Evaluate for parasitized red blood cells.
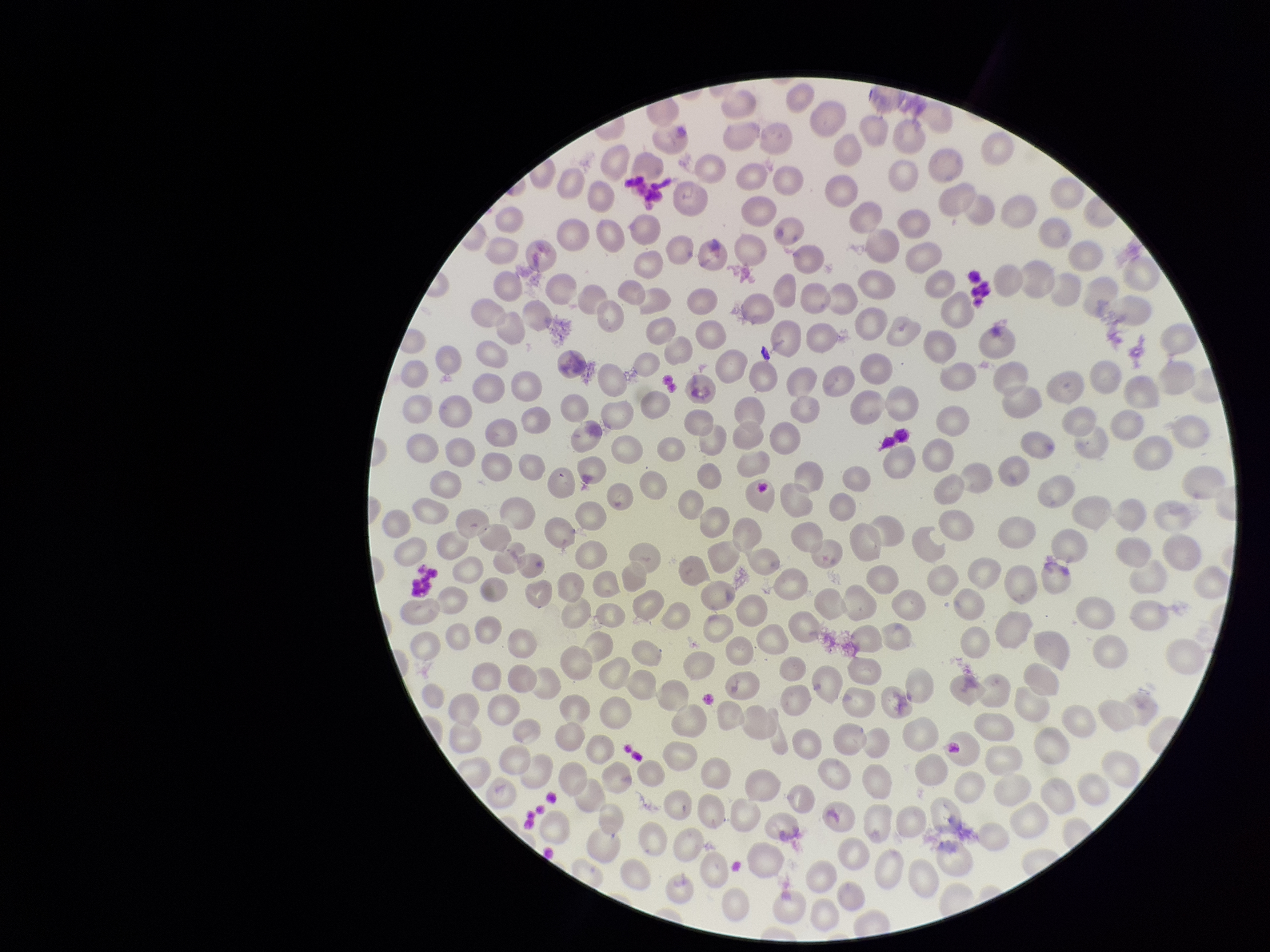
None identified.

Summary:
  - Image size: 1270×952 pixels
  - Capture: smartphone photograph through the microscope eyepiece
  - Parasitized red blood cell count: 0
  - Field of view: one from this slide
  - Preparation: thin smear
  - Patient malaria status: negative
  - Red blood cell count: 272
  - Stain: Giemsa